State which parasite is depicted.
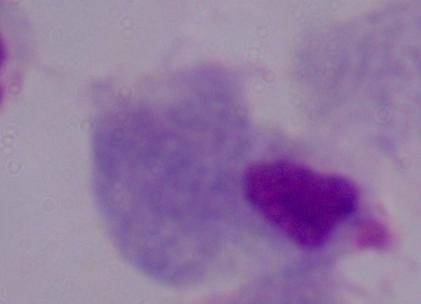

A trichomonad.

Captured at 1000x magnification. Photomicrograph.